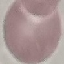

Summary:
  - Result: negative for malaria parasites
  - Image type: cell patch, automatically extracted from a larger field of view and resized to 64 × 64 pixels
  - Capture: smartphone through the microscope eyepiece
  - Stain: Giemsa
  - Preparation: thin smear